Classify this cell by malaria status.
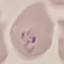
Uninfected.

Summary:
  - Stain: Giemsa
  - Capture: smartphone through the microscope eyepiece
  - Preparation: thin smear
  - Image type: cell patch, automatically extracted from a larger field of view and resized to 64 × 64 pixels